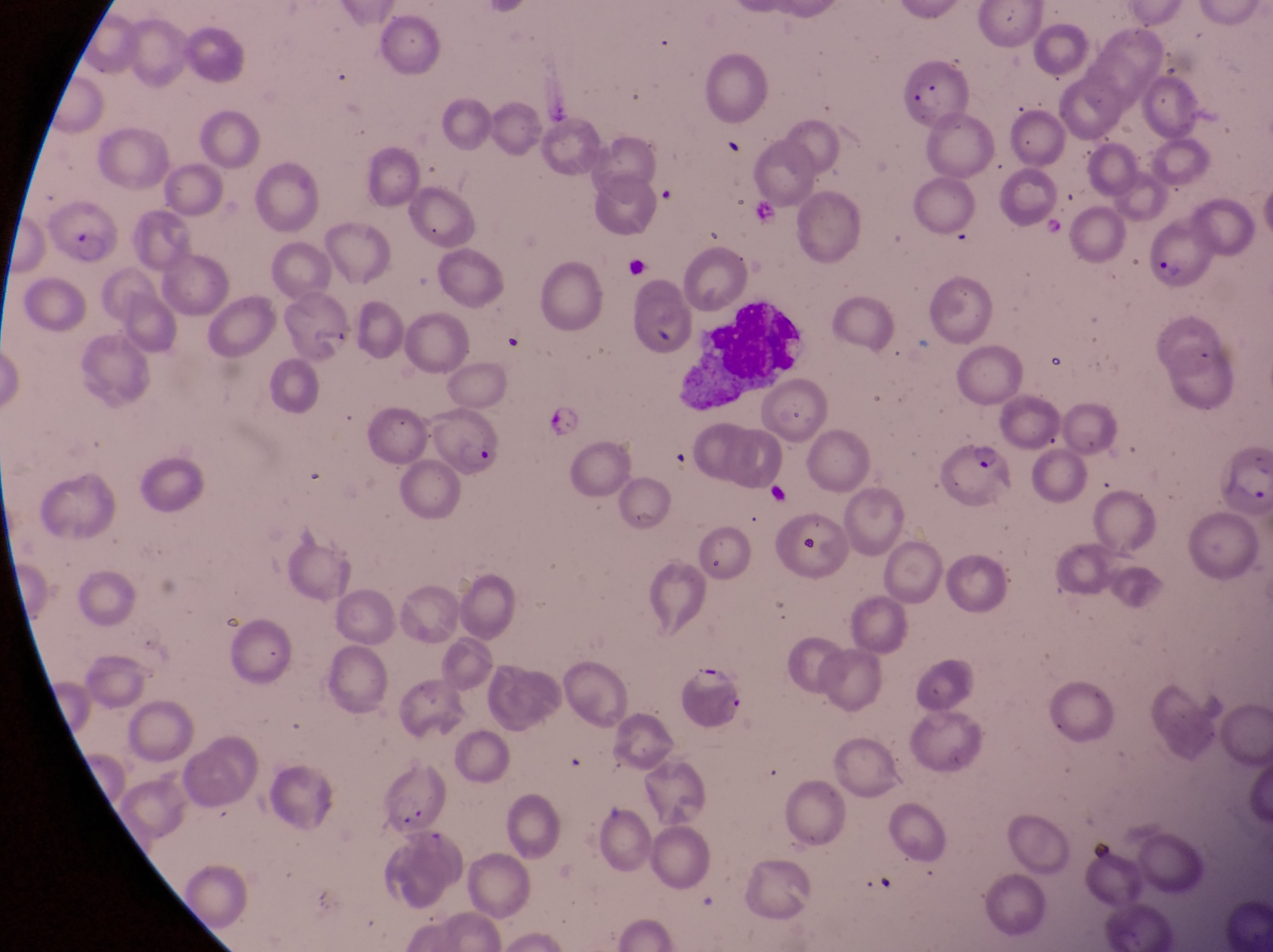

Approximate bounding boxes as (left, top, right, bottom) in pixels.
Summary:
  - Leukocyte locations: (687, 301, 808, 411)
  - Parasitised red blood cell locations: (901, 60, 973, 132), (43, 202, 123, 270), (1150, 222, 1219, 290), (764, 382, 833, 445), (427, 410, 505, 482), (938, 439, 1013, 507)
  - Capture: smartphone photograph through the eyepiece of an Olympus CX-23 microscope
  - Field of view: single
  - Preparation: thin blood film
  - Magnification: 1000x
  - Image size: 1273×952 pixels
  - Country: Uganda